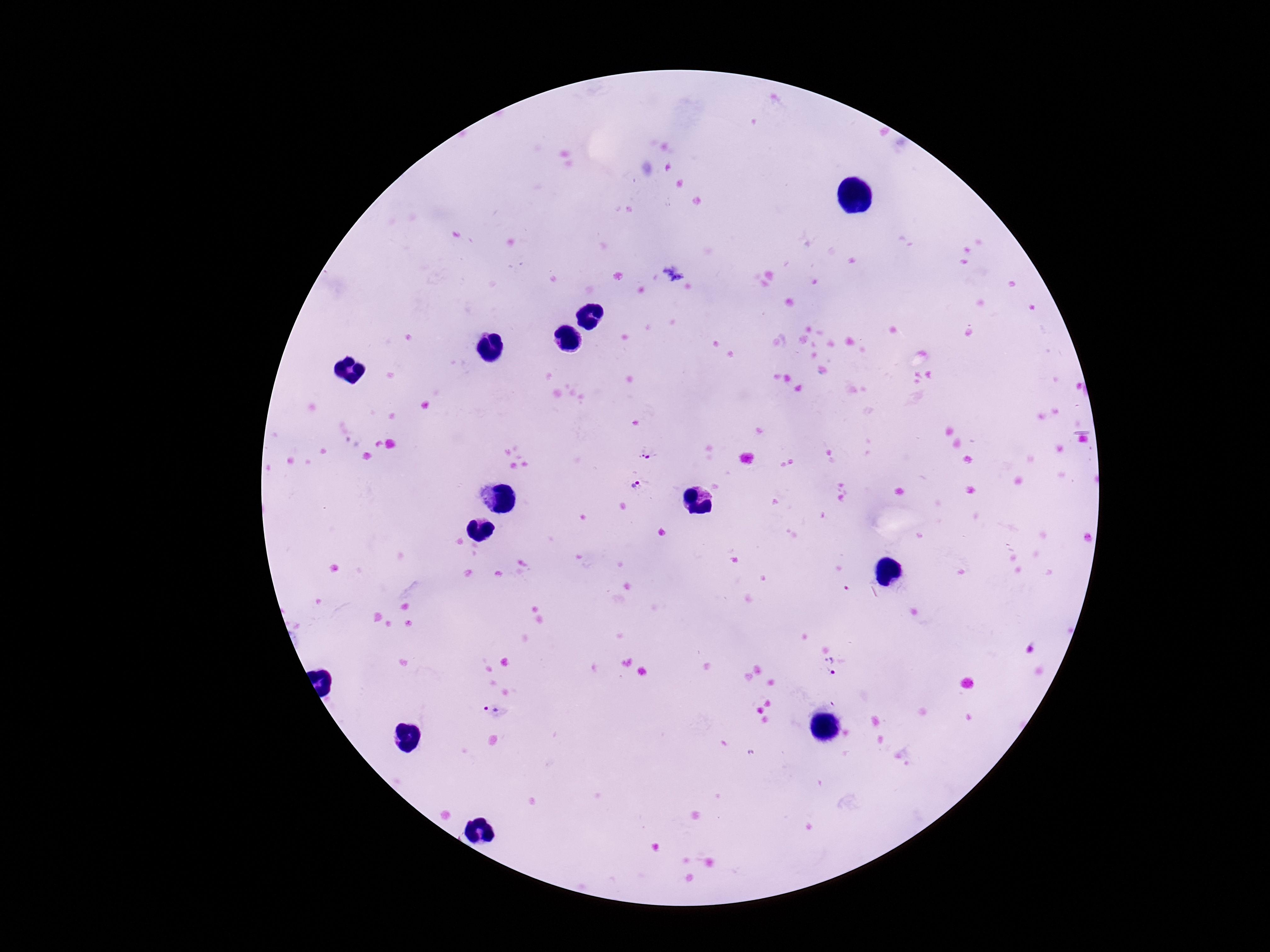
patient_malaria_status: positive
magnification: 100x
field_of_view: one from this slide
stain: Giemsa
image_size: 1270×952 pixels
capture: smartphone camera through the microscope eyepiece
plasmodium_parasite_locations: 'approximate object centers, in pixels from the top-left corner: (x=649, y=450), (x=637, y=487), (x=831, y=667), (x=490, y=713)'
preparation: thick blood smear